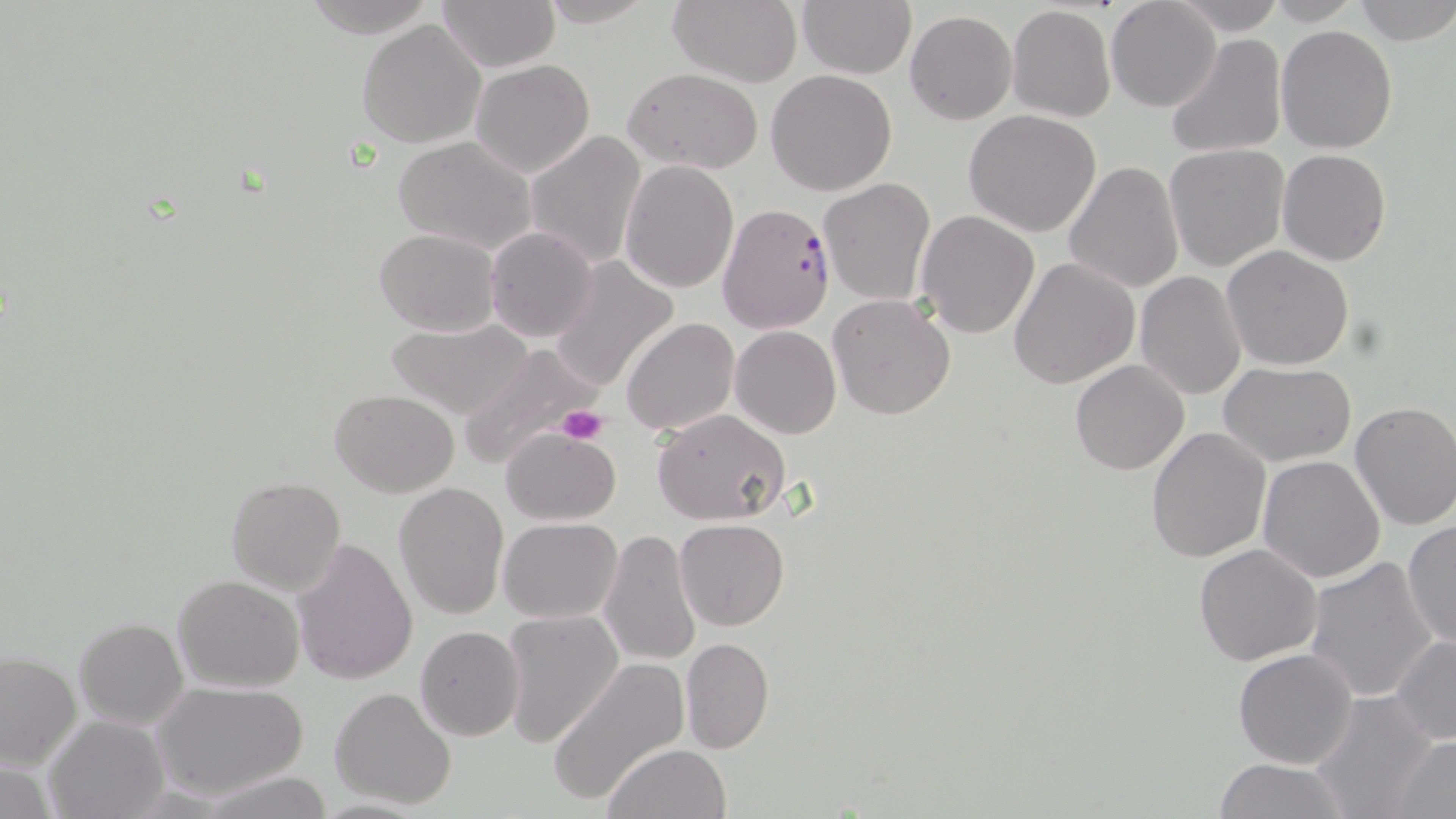

slide-level diagnosis = Plasmodium falciparum
uninfected red blood cell locations = approximate bounding boxes as (x1,y1)-(x2,y2) corner pairs in pixels: (535,0)-(661,27), (668,0)-(804,87), (796,0)-(917,78), (1170,0)-(1287,34), (1353,0)-(1456,45), (1106,1)-(1221,113), (439,2)-(559,71), (1007,5)-(1115,123), (904,11)-(1017,124), (357,20)-(485,148), (1276,25)-(1398,154), (1166,33)-(1288,159), (470,59)-(595,178), (625,66)-(764,173), (766,69)-(897,194), (963,110)-(1102,236), (525,130)-(647,272), (393,137)-(536,253), (1165,144)-(1290,271), (1278,148)-(1391,265), (621,160)-(740,293), (1063,161)-(1184,294), (818,178)-(936,307), (915,210)-(1040,338), (485,226)-(599,344), (374,228)-(498,336), (1223,247)-(1353,369), (1009,256)-(1139,390), (548,257)-(678,392), (1135,270)-(1247,399), (828,293)-(956,420), (384,318)-(538,418), (622,318)-(741,437), (730,326)-(842,439), (457,342)-(603,467), (1070,360)-(1189,475), (1220,362)-(1355,465), (330,389)-(458,495), (1349,400)-(1456,530), (651,409)-(790,525), (501,427)-(619,525), (1145,427)-(1269,562), (1257,455)-(1386,584), (225,476)-(345,595), (394,482)-(508,620), (497,517)-(622,622), (675,518)-(789,631), (1402,519)-(1455,650), (598,531)-(703,666), (291,537)-(419,685), (1194,543)-(1324,665), (1303,558)-(1440,703), (172,574)-(305,692), (498,610)-(623,749), (74,617)-(189,729), (413,625)-(524,741), (1390,635)-(1456,744), (680,637)-(773,755), (1233,648)-(1360,768), (1,652)-(80,770), (548,656)-(689,803), (151,681)-(307,800), (329,687)-(457,811), (1308,692)-(1439,819), (43,715)-(166,819), (1386,734)-(1456,818), (603,744)-(729,819), (1211,758)-(1354,818), (201,771)-(337,818)
image size = 1456×819 pixels
preparation = thin blood film
platelet locations = approximate bounding boxes as (x1,y1)-(x2,y2) corner pairs in pixels: (555,403)-(610,446)
field of view = single
Plasmodium falciparum-infected red blood cell locations = approximate bounding boxes as (x1,y1)-(x2,y2) corner pairs in pixels: (717,203)-(837,336)
modality = light microscopy
stain = May-Grünwald-Giemsa
magnification = 1000x